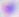
modality = micrograph
identification = Toxoplasma gondii
magnification = 400x